State which parasite is depicted.
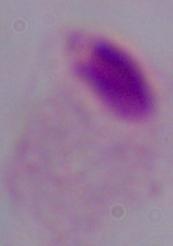
This is a trichomonad.

Summary:
  - Modality: photomicrograph
  - Magnification: 1000x